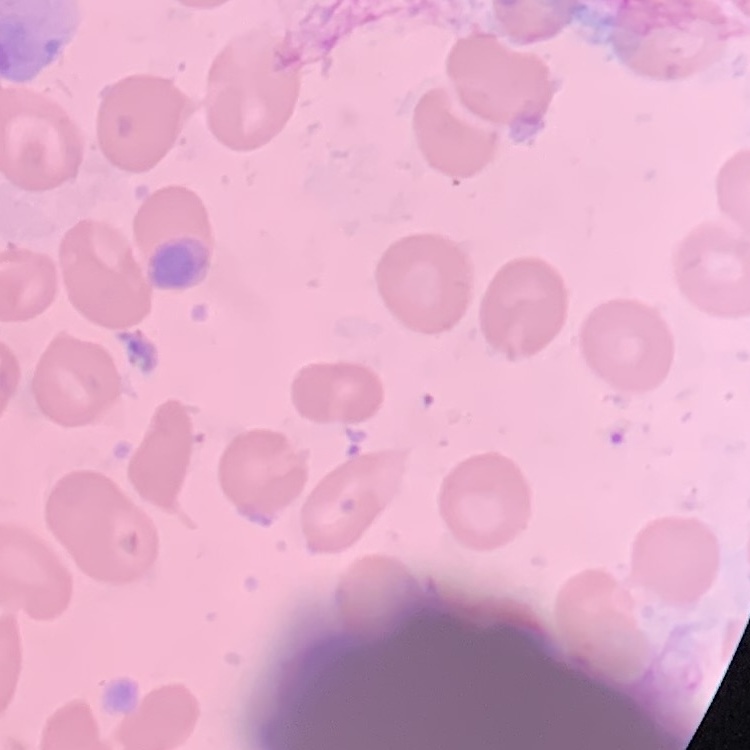

erythrocyte morphology = no rouleaux formation
image type = square crop of a larger photomicrograph
stain = Field's or Giemsa
preparation = thin blood film